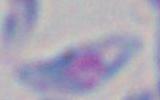
{
  "identification": "Toxoplasma gondii",
  "magnification": "1000x",
  "modality": "micrograph"
}